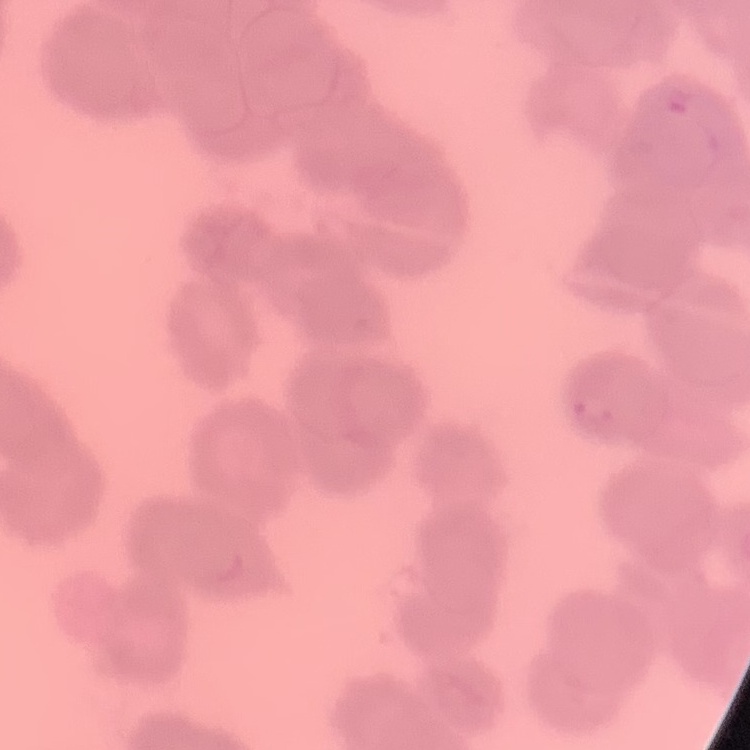

The red blood cells show rouleaux formation. Stained with either Field's or Giemsa. Thin blood smear. Square crop of a larger photomicrograph.